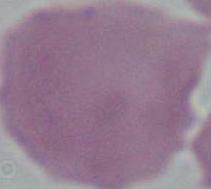

Summary:
  - Identification: red blood cell
  - Modality: micrograph
  - Magnification: 1000x